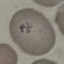
result = no malaria parasites detected
stain = Giemsa
capture = smartphone camera at the microscope eyepiece
preparation = thin blood film
image type = automatically extracted cell patch, resized to 64 × 64 pixels